Report the malaria status of this cell.
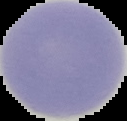

It is uninfected.

Summary:
  - Image size: 127×121 pixels
  - Preparation: thin blood smear
  - Image type: segmented cell region with the area outside set to black